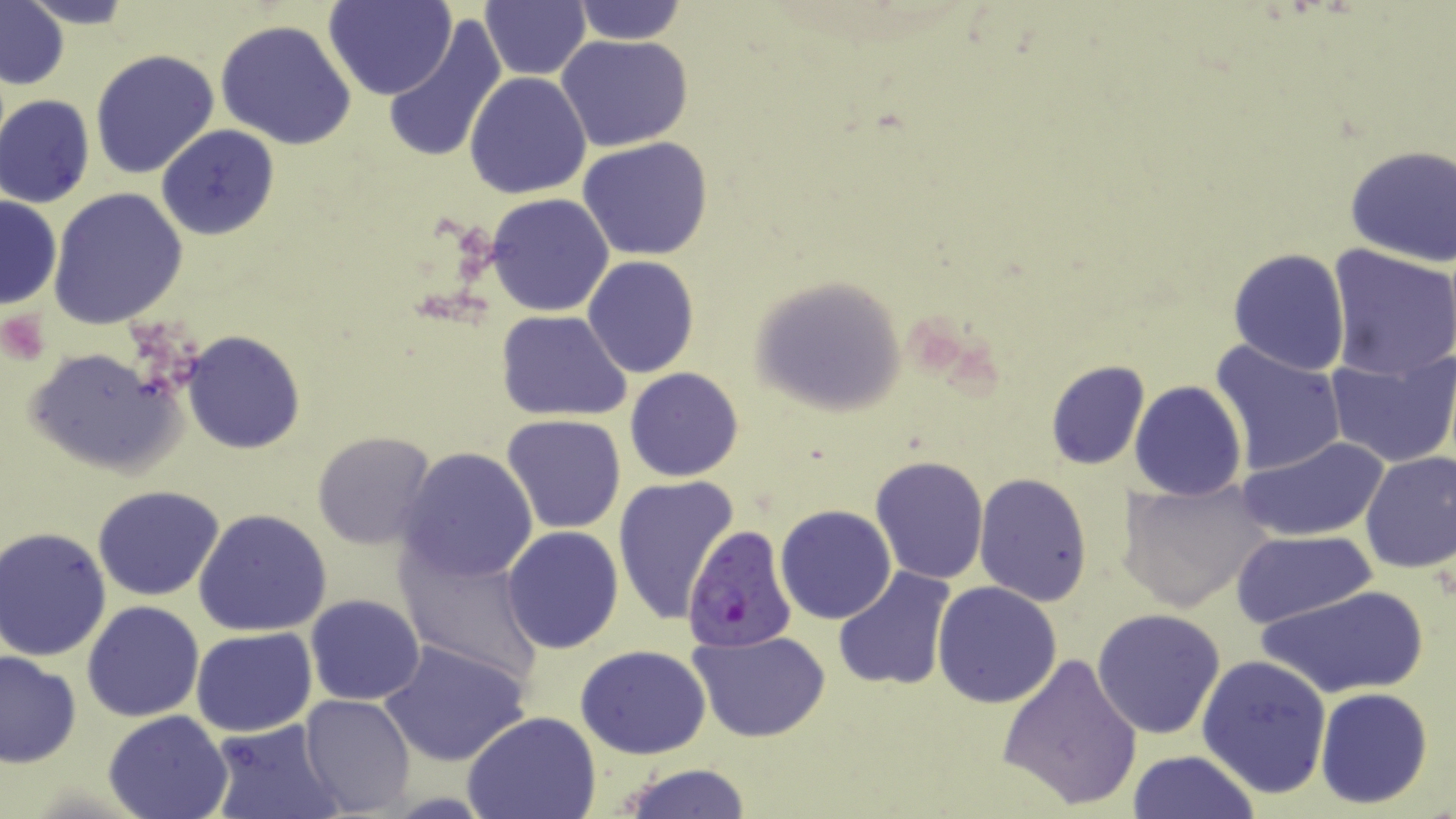 Approximate bounding boxes as (x1, y1, x2, y2) in pixels. Uninfected red blood cell locations: (15, 0, 141, 29), (326, 0, 456, 100), (1, 2, 68, 90), (480, 2, 591, 79), (568, 2, 690, 46), (383, 14, 508, 165), (212, 18, 358, 151), (556, 35, 695, 152), (91, 47, 220, 180), (464, 72, 592, 200), (1, 95, 95, 209), (156, 124, 279, 241), (578, 137, 712, 261), (1343, 142, 1456, 267), (50, 187, 187, 329), (486, 192, 615, 317), (0, 195, 62, 310), (1325, 245, 1455, 379), (1227, 247, 1349, 376), (583, 256, 699, 379), (750, 274, 907, 416), (497, 310, 631, 422), (184, 330, 305, 454), (1209, 339, 1347, 476), (24, 346, 184, 477), (1325, 348, 1456, 467), (1044, 359, 1151, 470), (625, 367, 744, 482), (1129, 380, 1247, 502), (502, 414, 627, 534), (311, 430, 438, 548), (1240, 434, 1391, 542), (397, 446, 540, 583), (1358, 450, 1455, 574), (869, 455, 988, 584), (973, 474, 1094, 608), (613, 475, 740, 625), (1119, 476, 1273, 611), (93, 486, 224, 601), (775, 505, 896, 624), (193, 507, 333, 638), (501, 527, 624, 653), (1, 528, 112, 661), (1230, 530, 1375, 630), (397, 545, 543, 686), (832, 566, 957, 691), (933, 581, 1061, 707), (1256, 583, 1430, 699), (305, 594, 426, 707), (80, 601, 204, 722), (1092, 609, 1227, 739), (190, 627, 317, 738), (690, 631, 831, 743), (380, 638, 530, 767), (574, 644, 713, 759), (0, 651, 80, 768), (996, 652, 1142, 810), (1197, 653, 1331, 799), (1314, 687, 1434, 808), (299, 693, 415, 814), (102, 710, 233, 819), (462, 711, 602, 819), (209, 720, 342, 819), (1125, 749, 1261, 819), (616, 764, 752, 818). Plasmodium falciparum-infected red blood cell locations: (682, 523, 797, 650). Slide-level diagnosis: Plasmodium falciparum. Light microscopy. 1000x magnification. Thin blood film. Single field of view. May-Grünwald-Giemsa-stained preparation. Image is 1456×819 pixels.